Comment on the morphology of the red blood cells.
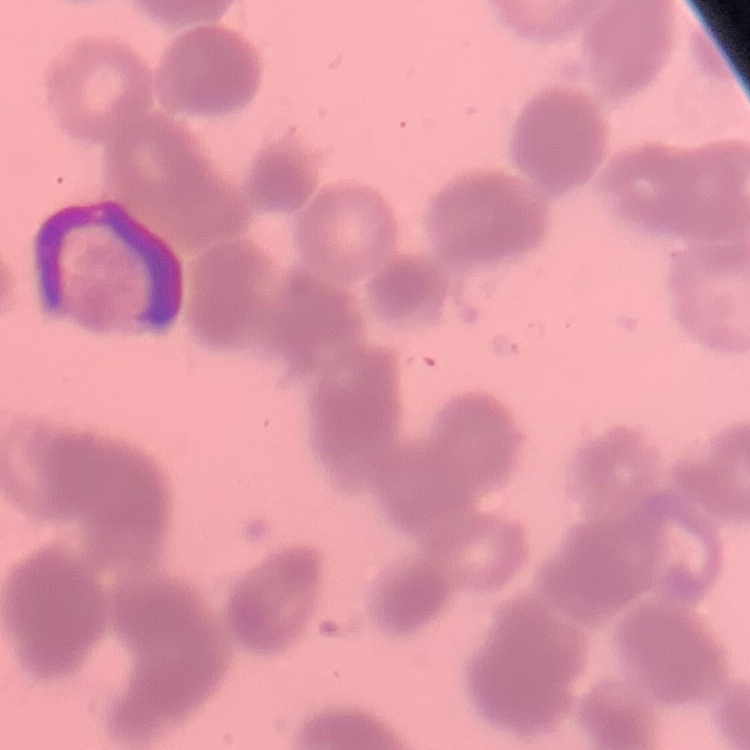
They show rouleaux formation.

image type = square crop of a larger photomicrograph
stain = Field's or Giemsa
preparation = thin blood film